Describe the morphology of the red blood cells.
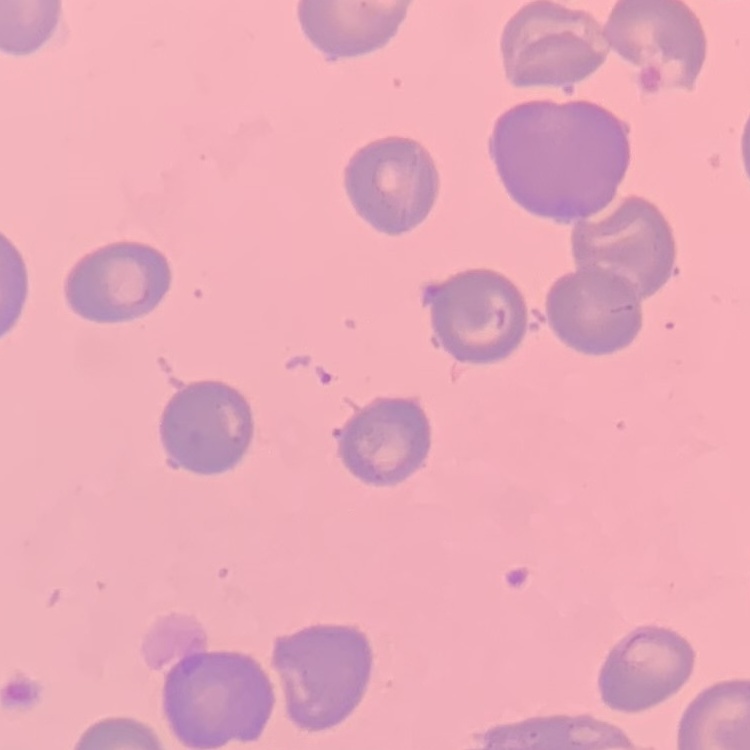
They show no rouleaux formation.

Thin blood film. Stained with either Field's or Giemsa. One tile cut from a larger photomicrograph.